Identify the cell.
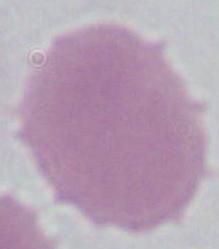

This is an erythrocyte.

{
  "modality": "micrograph",
  "magnification": "1000x"
}